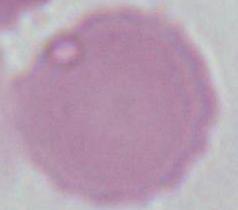
{
  "identification": "erythrocyte",
  "modality": "photomicrograph",
  "magnification": "1000x"
}